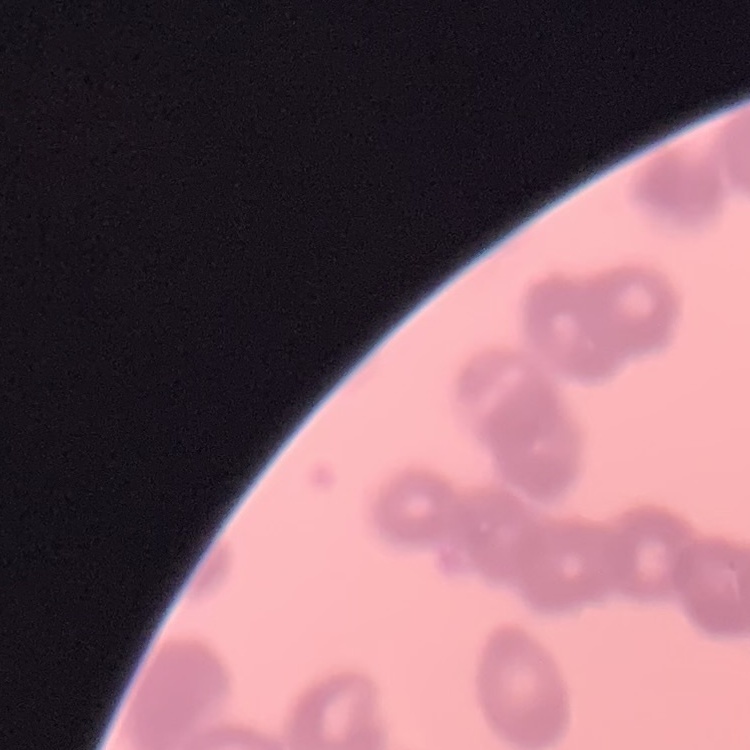
Summary:
  - Red blood cell morphology: rouleaux formation
  - Stain: Field's or Giemsa
  - Image type: square crop of a larger photomicrograph
  - Preparation: thin blood film